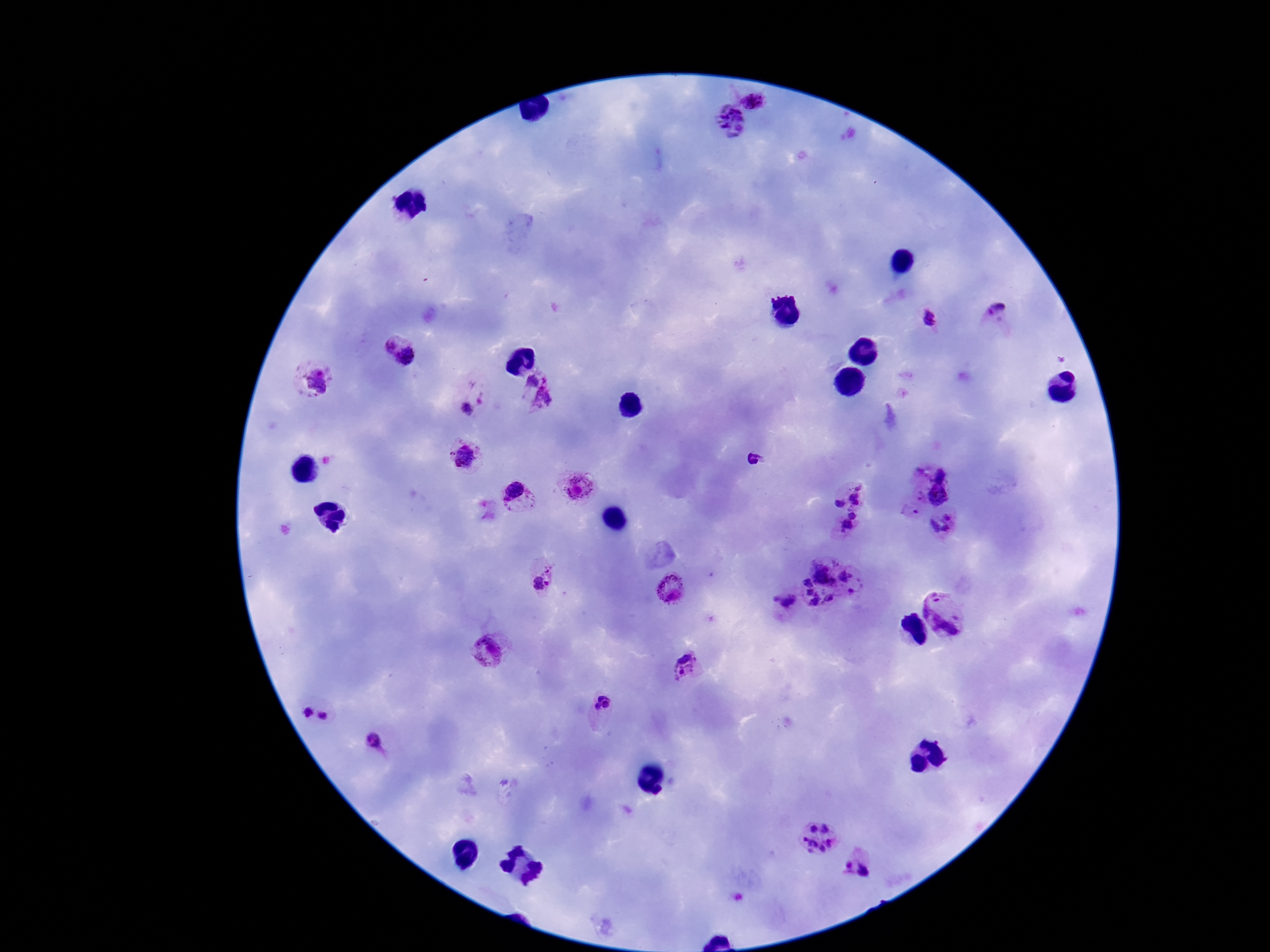
{
  "capture": "smartphone camera through the microscope eyepiece",
  "preparation": "thick blood smear",
  "patient_malaria_status": "infected",
  "magnification": "100x",
  "image_size": "1270×952 pixels",
  "stain": "Giemsa",
  "plasmodium_parasite_locations": "approximate centers as {x, y} in pixels: {755, 95}, {729, 124}, {998, 310}, {927, 318}, {387, 345}, {409, 357}, {313, 383}, {539, 392}, {469, 405}, {463, 455}, {753, 459}, {932, 461}, {574, 484}, {850, 492}, {916, 493}, {938, 497}, {519, 501}, {916, 512}, {849, 523}, {942, 525}, {542, 579}, {828, 584}, {670, 587}, {784, 602}, {947, 611}, {490, 650}, {684, 667}, {605, 706}, {318, 716}, {370, 742}, {814, 836}, {855, 864}",
  "field_of_view": "single"
}